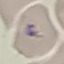

Result: no malaria parasites seen. Giemsa stain. Thin smear of blood. Acquired by smartphone through the microscope eyepiece. Automatically extracted cell patch, resized to 64 × 64 pixels.